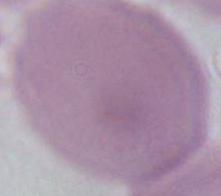
Summary:
  - Magnification: 1000x
  - Modality: photomicrograph
  - Identification: red blood cell